Describe the morphology of the red blood cells.
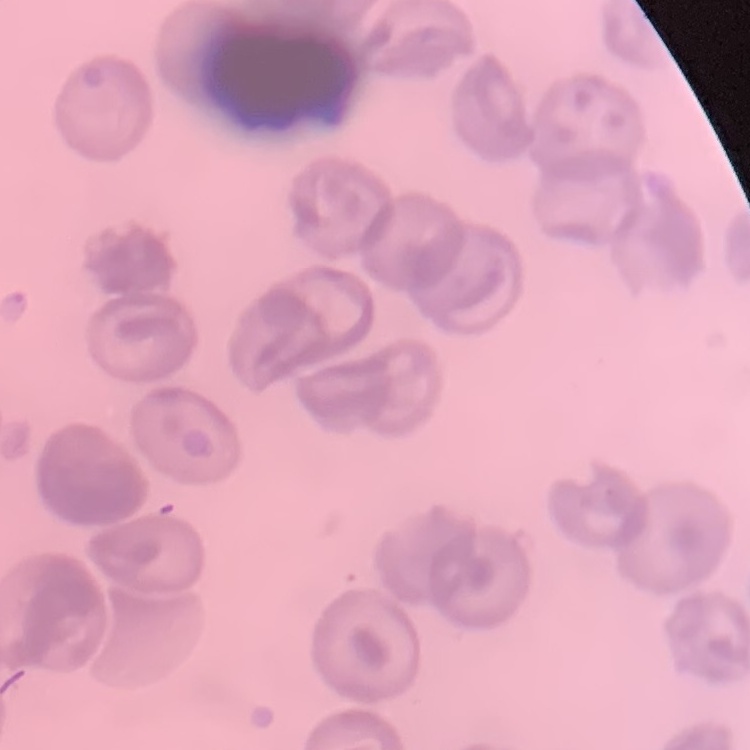

They show no rouleaux formation.

Field's or Giemsa stain. One tile cut from a larger photomicrograph. Thin blood film.